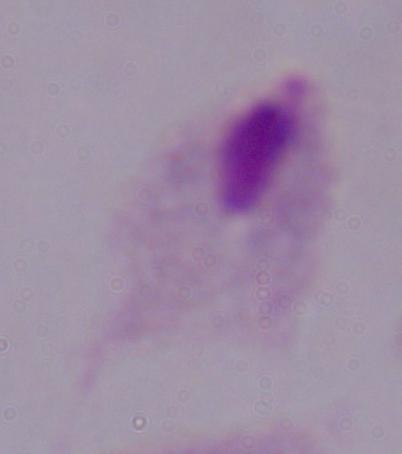

Captured at 1000x magnification. Micrograph. A trichomonad is shown.